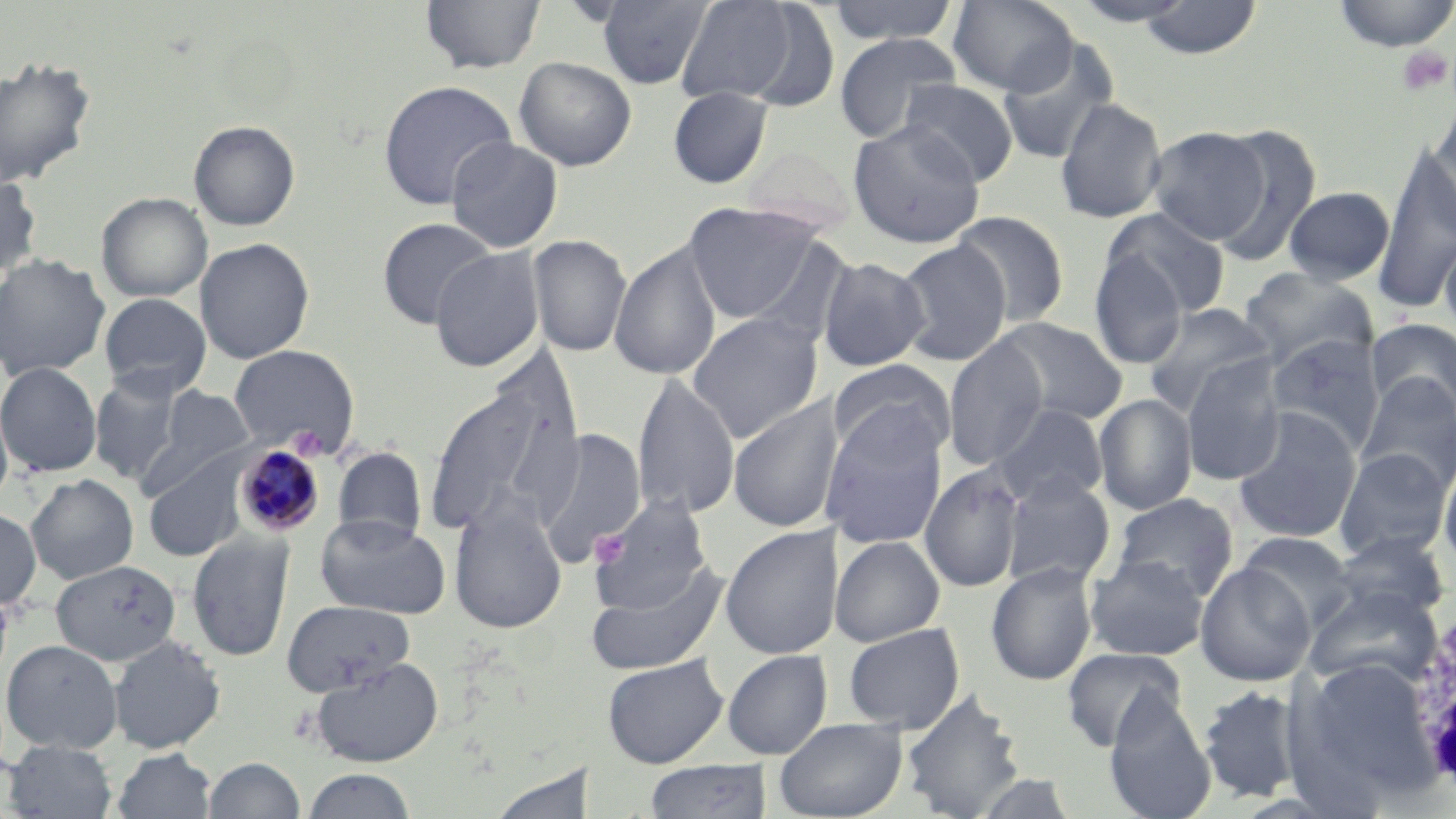

Approximate bounding boxes as named x1/y1/x2/y2 corners in pixels. Uninfected red blood cell locations: (x1=420, y1=0, x2=546, y2=75), (x1=595, y1=0, x2=715, y2=89), (x1=825, y1=0, x2=961, y2=45), (x1=947, y1=0, x2=1078, y2=96), (x1=1067, y1=0, x2=1201, y2=26), (x1=1331, y1=0, x2=1456, y2=52), (x1=674, y1=1, x2=802, y2=106), (x1=740, y1=1, x2=843, y2=112), (x1=1136, y1=1, x2=1263, y2=60), (x1=833, y1=32, x2=963, y2=143), (x1=997, y1=38, x2=1119, y2=166), (x1=0, y1=55, x2=98, y2=188), (x1=513, y1=56, x2=637, y2=171), (x1=377, y1=79, x2=518, y2=210), (x1=898, y1=79, x2=1020, y2=186), (x1=667, y1=86, x2=773, y2=189), (x1=1055, y1=96, x2=1167, y2=224), (x1=1428, y1=103, x2=1456, y2=231), (x1=189, y1=120, x2=300, y2=231), (x1=847, y1=120, x2=986, y2=249), (x1=1146, y1=126, x2=1271, y2=244), (x1=1210, y1=126, x2=1321, y2=265), (x1=445, y1=136, x2=564, y2=253), (x1=740, y1=144, x2=858, y2=235), (x1=1373, y1=145, x2=1456, y2=314), (x1=0, y1=170, x2=42, y2=279), (x1=1283, y1=186, x2=1396, y2=284), (x1=96, y1=192, x2=212, y2=302), (x1=684, y1=202, x2=819, y2=323), (x1=1102, y1=207, x2=1231, y2=319), (x1=950, y1=211, x2=1070, y2=327), (x1=376, y1=217, x2=499, y2=329), (x1=527, y1=234, x2=632, y2=358), (x1=1440, y1=235, x2=1456, y2=339), (x1=195, y1=237, x2=315, y2=365), (x1=895, y1=239, x2=1012, y2=367), (x1=609, y1=242, x2=722, y2=382), (x1=429, y1=247, x2=545, y2=372), (x1=1088, y1=251, x2=1189, y2=370), (x1=0, y1=254, x2=111, y2=379), (x1=817, y1=256, x2=930, y2=372), (x1=1238, y1=267, x2=1379, y2=372), (x1=99, y1=293, x2=212, y2=396), (x1=1142, y1=302, x2=1276, y2=418), (x1=686, y1=312, x2=824, y2=443), (x1=990, y1=317, x2=1128, y2=426), (x1=1366, y1=318, x2=1456, y2=416), (x1=1266, y1=334, x2=1385, y2=456), (x1=943, y1=338, x2=1049, y2=470), (x1=229, y1=345, x2=358, y2=455), (x1=1179, y1=355, x2=1286, y2=487), (x1=827, y1=359, x2=955, y2=466), (x1=0, y1=361, x2=102, y2=477), (x1=88, y1=370, x2=189, y2=486), (x1=1356, y1=373, x2=1456, y2=494), (x1=422, y1=374, x2=582, y2=541), (x1=631, y1=374, x2=741, y2=520), (x1=137, y1=384, x2=258, y2=498), (x1=727, y1=394, x2=845, y2=533), (x1=1094, y1=394, x2=1198, y2=515), (x1=0, y1=397, x2=14, y2=513), (x1=988, y1=403, x2=1108, y2=509), (x1=1232, y1=407, x2=1363, y2=544), (x1=821, y1=408, x2=949, y2=549), (x1=534, y1=428, x2=647, y2=564), (x1=332, y1=447, x2=427, y2=546), (x1=1334, y1=448, x2=1453, y2=561), (x1=143, y1=453, x2=249, y2=562), (x1=1438, y1=454, x2=1456, y2=575), (x1=919, y1=463, x2=1028, y2=593), (x1=25, y1=473, x2=139, y2=584), (x1=999, y1=474, x2=1116, y2=589), (x1=586, y1=493, x2=713, y2=615), (x1=1111, y1=493, x2=1239, y2=601), (x1=448, y1=500, x2=567, y2=634), (x1=0, y1=507, x2=41, y2=611), (x1=314, y1=514, x2=451, y2=619), (x1=719, y1=524, x2=843, y2=659), (x1=1237, y1=530, x2=1356, y2=629), (x1=1329, y1=530, x2=1452, y2=622), (x1=187, y1=534, x2=294, y2=662), (x1=829, y1=535, x2=945, y2=647), (x1=1085, y1=555, x2=1210, y2=661), (x1=50, y1=559, x2=181, y2=666), (x1=585, y1=561, x2=730, y2=676), (x1=985, y1=562, x2=1098, y2=686), (x1=1195, y1=562, x2=1316, y2=687), (x1=1305, y1=585, x2=1440, y2=690), (x1=280, y1=599, x2=416, y2=696), (x1=842, y1=623, x2=965, y2=733), (x1=108, y1=635, x2=226, y2=754), (x1=1, y1=639, x2=123, y2=754), (x1=1061, y1=647, x2=1187, y2=751), (x1=722, y1=650, x2=832, y2=760), (x1=602, y1=655, x2=728, y2=768), (x1=310, y1=657, x2=444, y2=767), (x1=1300, y1=657, x2=1435, y2=788), (x1=1197, y1=685, x2=1303, y2=802), (x1=900, y1=688, x2=1026, y2=819), (x1=1102, y1=694, x2=1217, y2=819), (x1=774, y1=717, x2=907, y2=819), (x1=3, y1=740, x2=118, y2=818), (x1=112, y1=748, x2=216, y2=819), (x1=204, y1=757, x2=305, y2=818), (x1=643, y1=760, x2=772, y2=819), (x1=301, y1=768, x2=417, y2=818). White blood cell locations: (x1=1405, y1=599, x2=1456, y2=796). Platelet locations: (x1=1395, y1=46, x2=1453, y2=96), (x1=287, y1=424, x2=330, y2=460). Plasmodium malariae-infected red blood cell locations: (x1=233, y1=444, x2=325, y2=537). Slide-level diagnosis: Plasmodium malariae. May-Grünwald-Giemsa-stained preparation. Thin blood smear. Light microscopy. One field of a larger specimen. Captured at 1000x magnification. Image is 1456×819 pixels.